Point out each Plasmodium parasite.
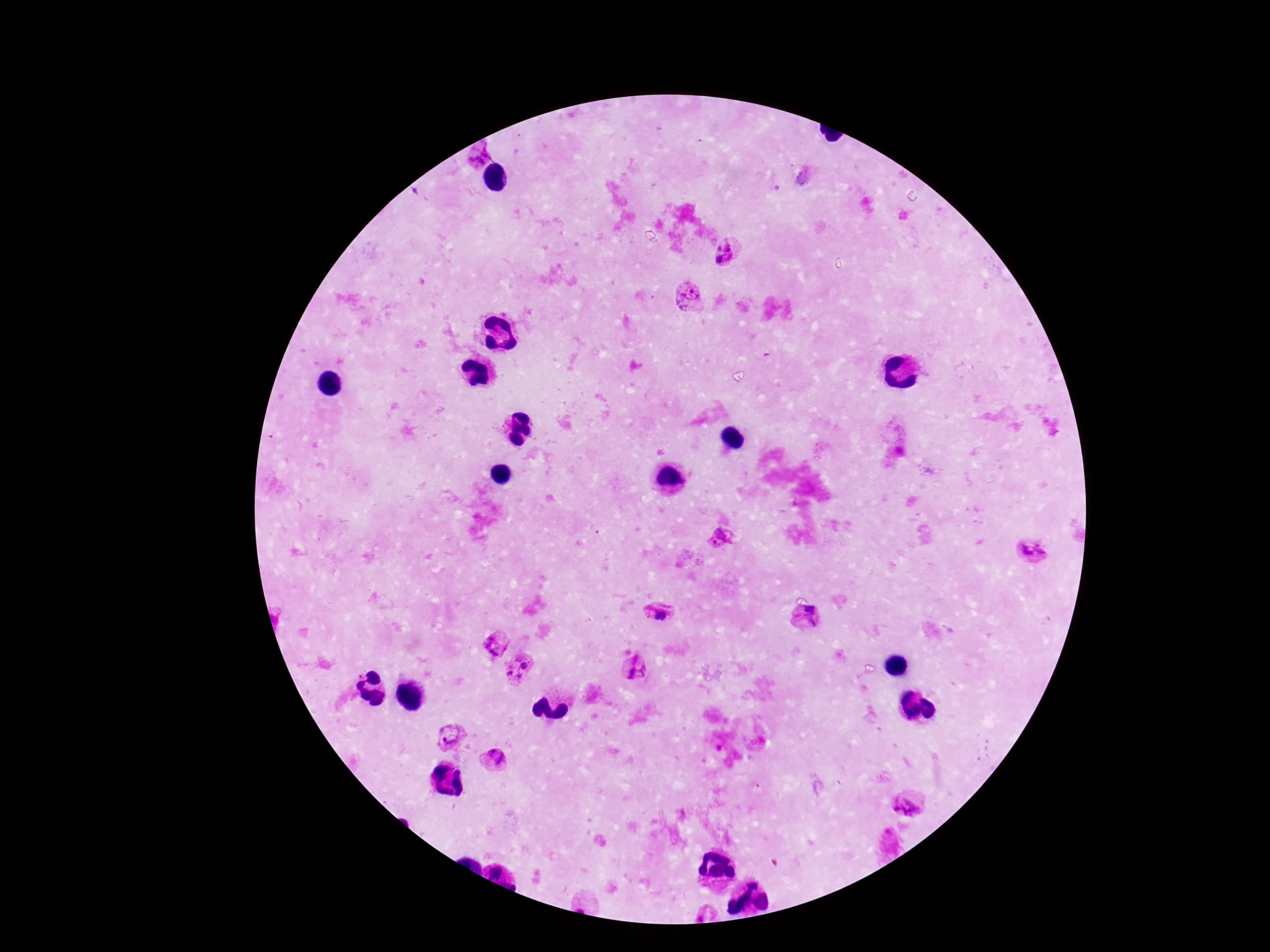
Approximate centers as {x, y} in pixels.
Plasmodium parasites: {481, 151}, {728, 245}, {718, 248}, {718, 260}, {688, 298}, {721, 539}, {1032, 552}, {661, 611}, {808, 618}, {496, 644}, {525, 664}, {637, 669}, {507, 673}, {519, 676}, {448, 733}, {493, 760}, {909, 802}.

{
  "image_size": "1270×952 pixels",
  "magnification": "100x",
  "patient_malaria_status": "positive",
  "stain": "Giemsa",
  "field_of_view": "single",
  "capture": "smartphone camera through the microscope eyepiece",
  "preparation": "thick blood smear"
}